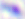

Summary:
  - Modality: micrograph
  - Identification: Toxoplasma gondii
  - Magnification: 400x